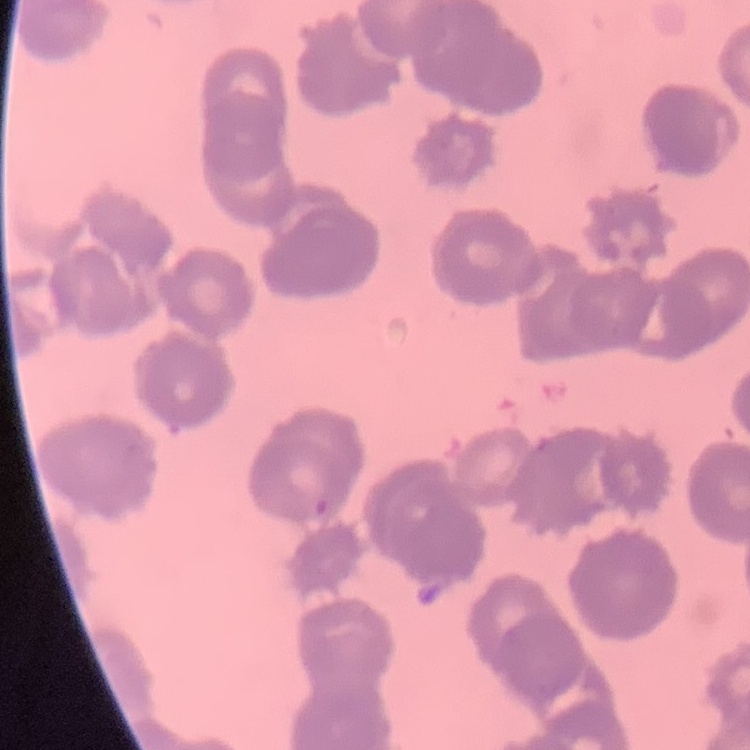

erythrocyte_morphology: rouleaux formation
preparation: thin peripheral smear
image_type: square crop of a larger photomicrograph
stain: Field's or Giemsa